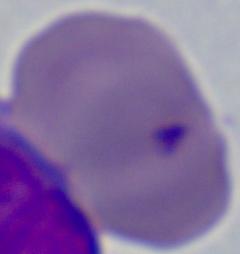
Micrograph. Captured at 1000x magnification. A Babesia parasite is seen.